Classify this cell by malaria status.
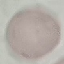

Uninfected.

preparation = thin blood smear
stain = Giemsa
capture = smartphone camera at the microscope eyepiece
image type = cell patch, automatically extracted from a larger field of view and resized to 64 × 64 pixels